Assess for Plasmodium parasites.
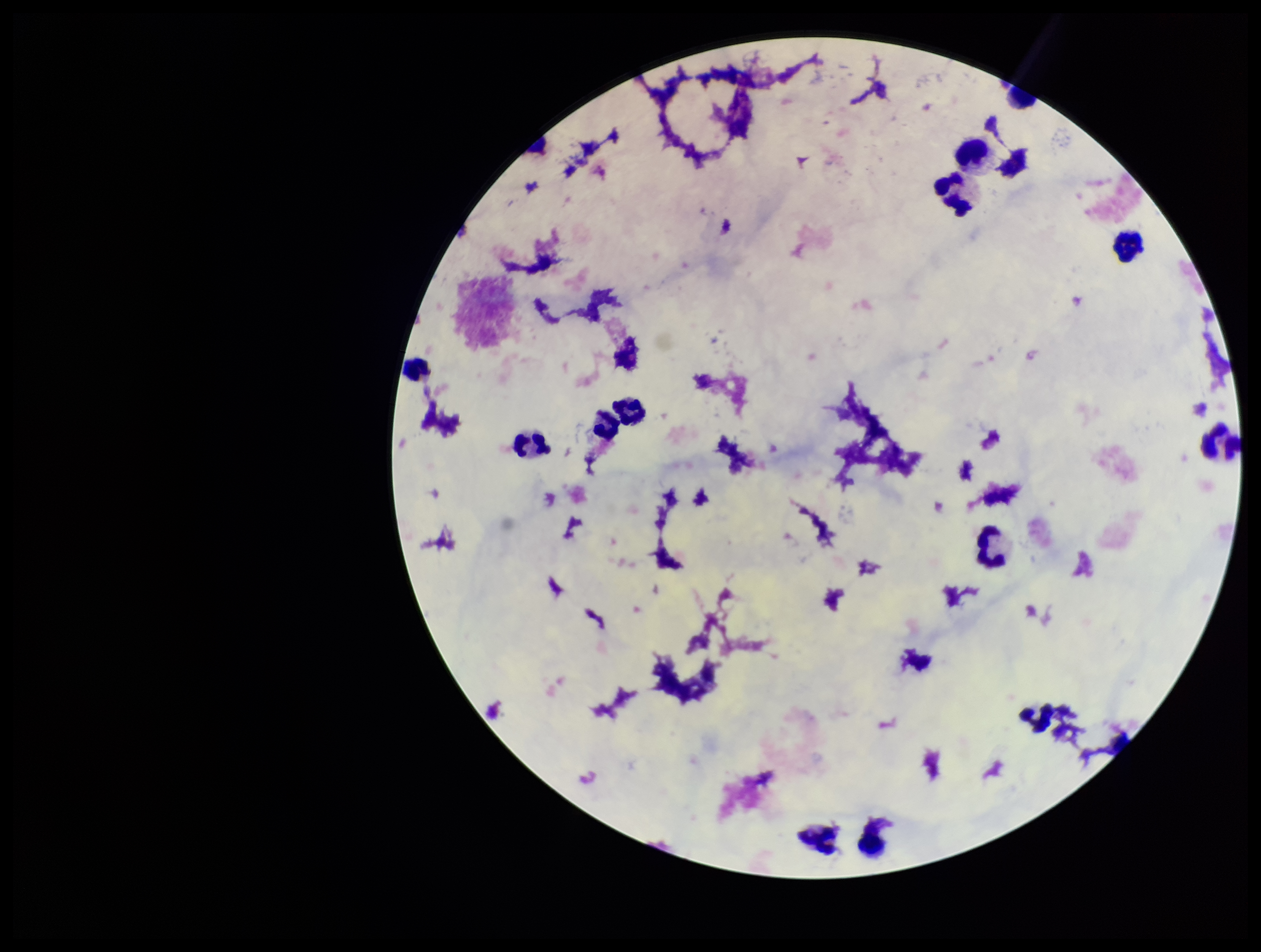

None seen.

capture = smartphone photograph through the microscope eyepiece
stain = Giemsa
field of view = single
leukocyte count = 13
parasite count = 0
patient malaria status = negative
image size = 1261×952 pixels
preparation = thick